Assess this cell for malaria.
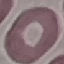
Uninfected.

Cell patch, automatically extracted from a larger field of view and resized to 64 × 64 pixels. Giemsa stain. Photographed with a smartphone camera at the microscope eyepiece. Thin smear of blood.